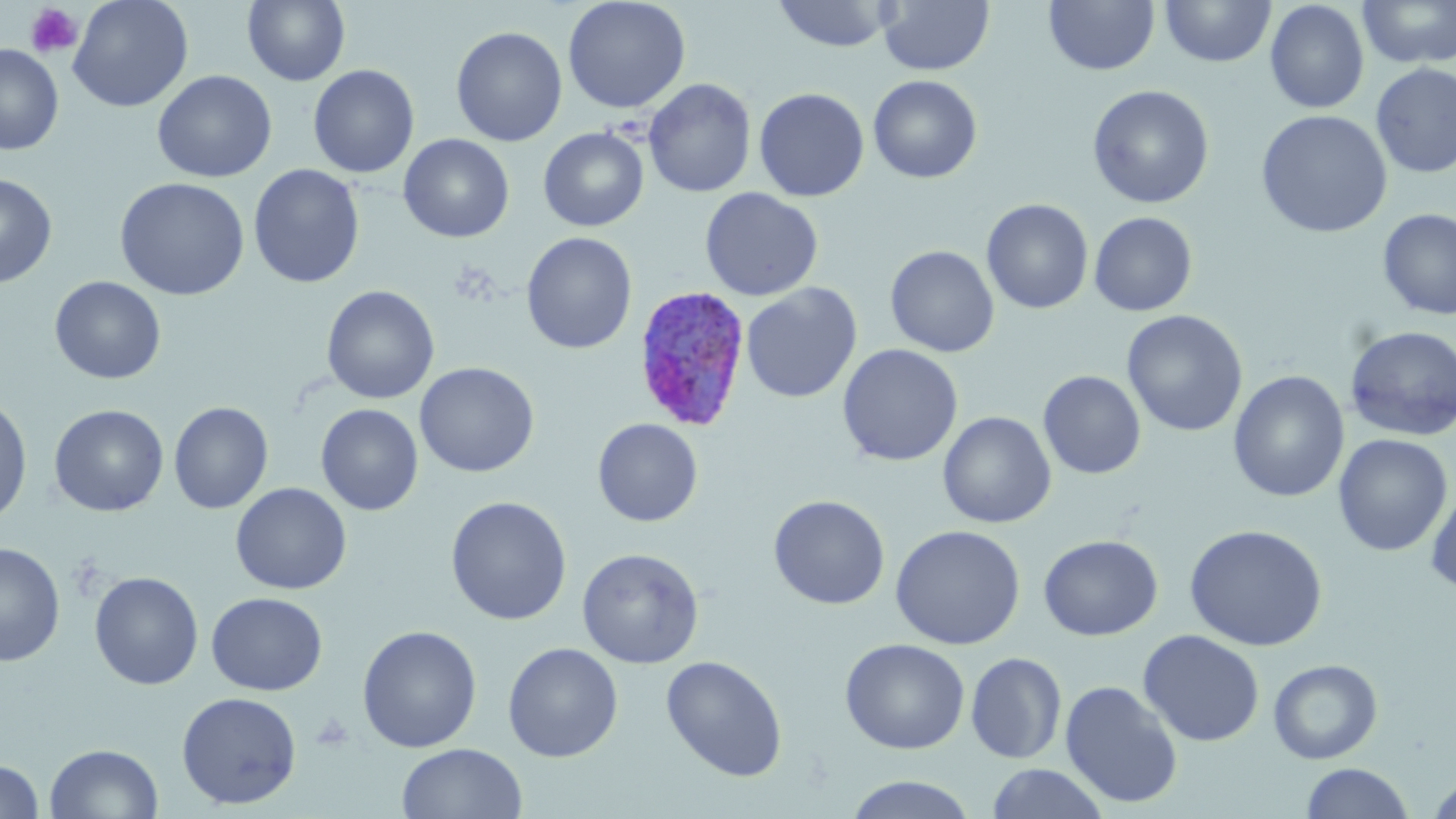

Approximate bounding boxes as (x1,y1)-(x2,y2) corner pairs in pixels. Uninfected red blood cell locations: (67,0)-(193,112), (243,0)-(350,86), (562,0)-(691,114), (771,0)-(899,52), (878,0)-(994,76), (1044,0)-(1160,76), (1358,0)-(1456,70), (1160,1)-(1276,68), (1265,1)-(1369,114), (450,26)-(567,146), (0,44)-(64,155), (1371,62)-(1456,178), (308,65)-(419,178), (152,70)-(277,182), (868,75)-(982,183), (643,78)-(756,197), (1087,84)-(1214,209), (754,87)-(869,202), (1255,109)-(1393,238), (538,127)-(649,231), (398,133)-(515,242), (248,164)-(364,288), (0,173)-(57,288), (114,177)-(250,301), (700,187)-(823,301), (981,198)-(1093,314), (1378,208)-(1456,320), (1089,212)-(1198,316), (521,232)-(637,354), (885,245)-(1000,357), (49,275)-(166,384), (740,282)-(862,403), (321,285)-(439,404), (1122,310)-(1248,437), (1344,325)-(1456,441), (837,344)-(963,467), (415,362)-(539,477), (1038,370)-(1146,479), (1228,370)-(1350,502), (952,393)-(1126,510), (0,394)-(33,527), (169,401)-(273,514), (49,404)-(169,517), (316,404)-(423,516), (938,411)-(1056,528), (592,418)-(703,527), (1333,434)-(1453,557), (1425,481)-(1456,598), (230,482)-(352,594), (768,495)-(890,609), (445,496)-(572,625), (891,524)-(1026,650), (1184,524)-(1328,651), (1038,534)-(1163,641), (0,541)-(65,667), (577,548)-(703,668), (89,571)-(204,690), (206,592)-(327,695), (357,625)-(482,753), (1138,629)-(1264,747), (839,638)-(970,754), (503,642)-(623,762), (966,652)-(1067,764), (661,655)-(787,782), (1268,658)-(1383,764), (1060,679)-(1184,809), (176,691)-(302,810), (45,743)-(163,819), (397,743)-(527,819), (0,760)-(44,818), (1300,762)-(1414,819), (985,763)-(1110,819), (845,774)-(977,819), (1425,774)-(1456,819). Platelet locations: (25,3)-(83,59). Plasmodium ovale-infected red blood cell locations: (632,285)-(752,433). Slide-level diagnosis: Plasmodium ovale. May-Grünwald-Giemsa stain. Image is 1456×819 pixels. Single field of view. Light microscopy. Thin blood smear. Captured at 1000x magnification.